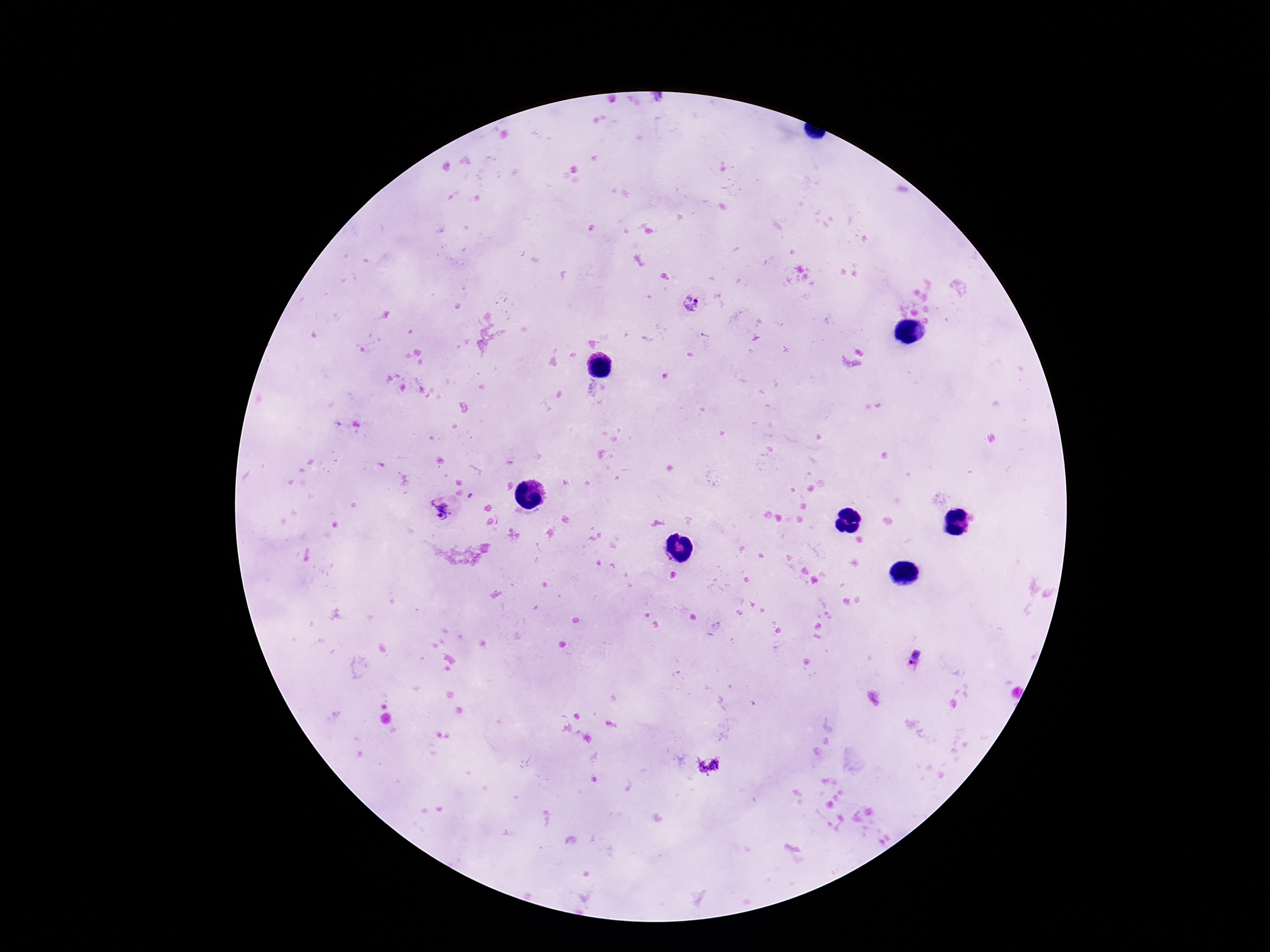

Approximate object centers, in pixels from the top-left corner.
Summary:
  - Plasmodium parasite locations: (x=690, y=300), (x=442, y=513), (x=915, y=658)
  - Capture: smartphone camera through the microscope eyepiece
  - Patient malaria status: infected
  - Stain: Giemsa
  - Image size: 1270×952 pixels
  - Preparation: thick peripheral-blood smear
  - Field of view: one from this slide
  - Magnification: 100x